Report the malaria status of this cell.
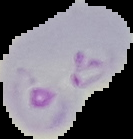

It is parasitized.

Summary:
  - Image type: cell region segmented out of the field of view; surrounding area masked to black
  - Preparation: thin blood film
  - Image size: 133×139 pixels